Report the malaria status of this cell.
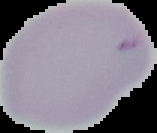
Parasitized.

Image is 157×133 pixels. From a thin blood film. Segmented cell region on a black background.